Assess the morphology of the erythrocytes.
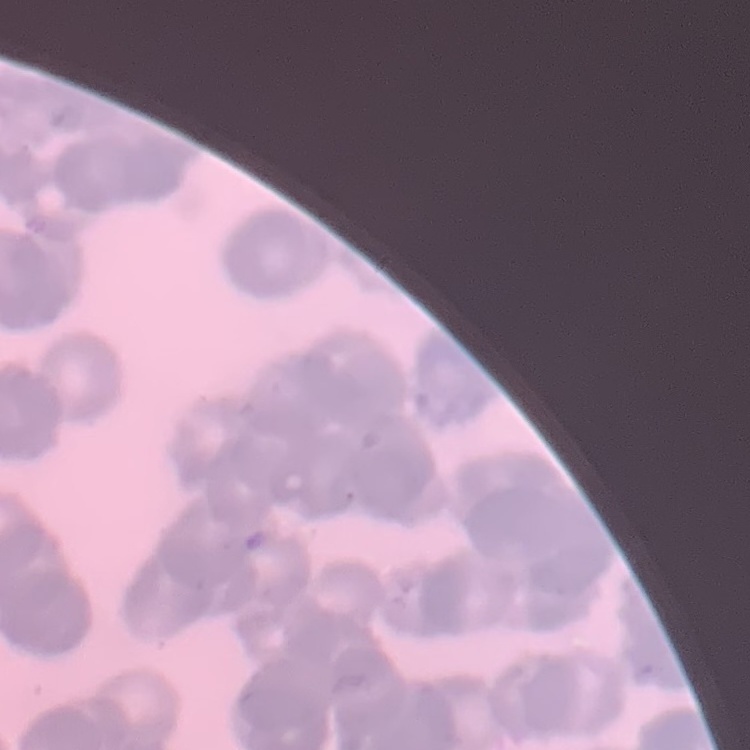

Rouleaux formation.

Summary:
  - Preparation: thin blood smear
  - Image type: one tile cut from a larger photomicrograph
  - Stain: Field's or Giemsa